Find each parasitized red blood cell.
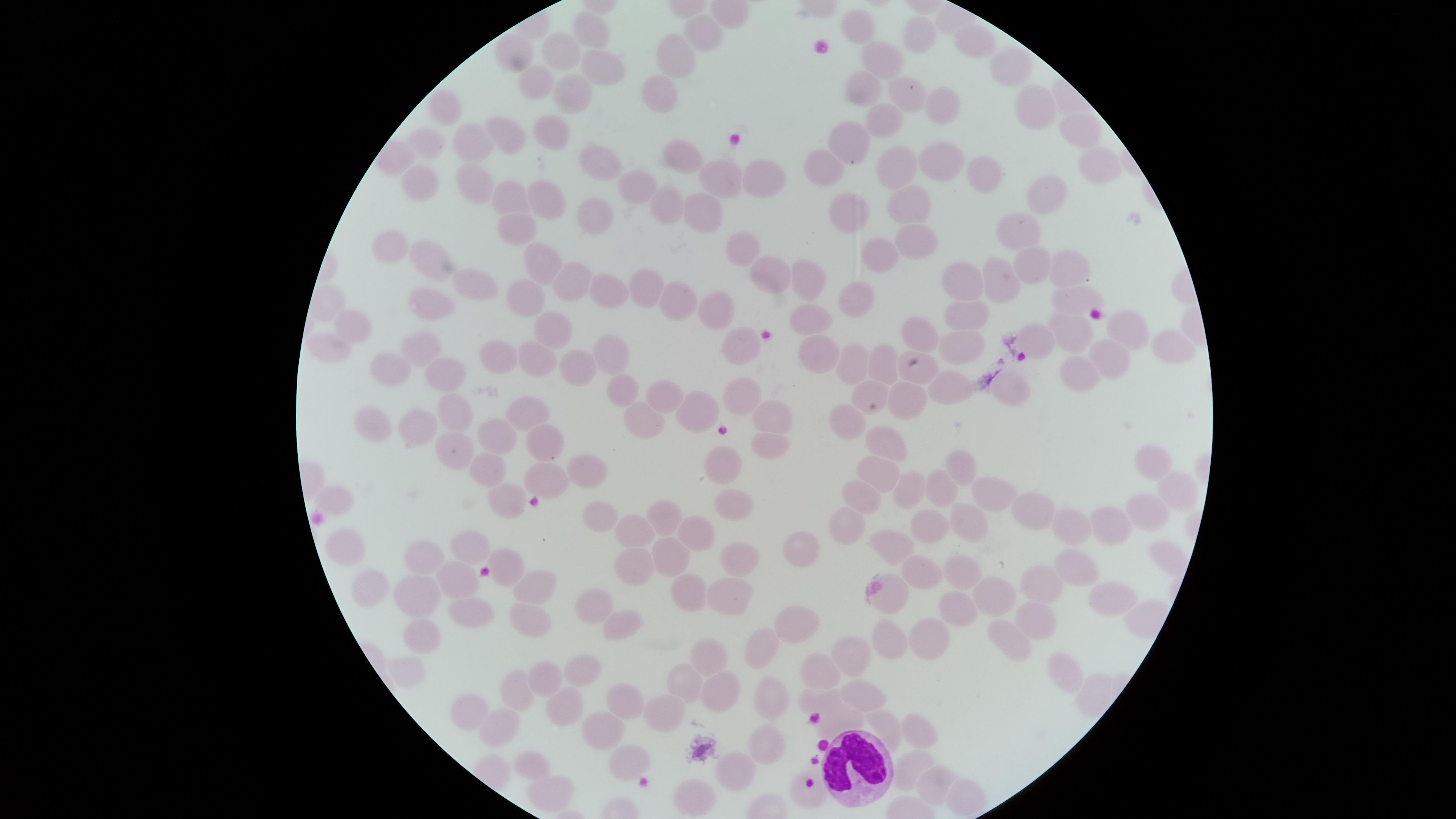
No parasitized red blood cells identified.

white blood cells = approximate marker points as {x, y} in pixels: {856, 768}
visible region = circular
field of view = single
capture = smartphone photograph through the microscope eyepiece
uninfected red blood cells = approximate marker points as {x, y} in pixels: {862, 23}, {702, 33}, {590, 34}, {915, 36}, {973, 41}, {556, 50}, {518, 51}, {678, 56}, {880, 58}, {999, 61}, {603, 64}, {660, 83}, {531, 84}, {865, 91}, {902, 91}, {565, 95}, {445, 102}, {1029, 102}, {929, 103}, {885, 118}, {553, 130}, {1076, 131}, {859, 137}, {428, 140}, {473, 141}, {508, 142}, {678, 147}, {897, 158}, {939, 159}, {833, 163}, {599, 164}, {761, 167}, {980, 170}, {718, 171}, {419, 179}, {473, 180}, {635, 182}, {1049, 193}, {514, 195}, {669, 198}, {544, 200}, {857, 206}, {910, 206}, {704, 207}, {596, 212}, {517, 226}, {1018, 226}, {910, 239}, {741, 245}, {393, 248}, {877, 256}, {428, 258}, {545, 262}, {1035, 265}, {1069, 265}, {763, 269}, {809, 272}, {964, 278}, {1001, 278}, {572, 281}, {483, 282}, {650, 287}, {613, 288}, {522, 295}, {1071, 295}, {856, 297}, {427, 300}, {680, 304}, {715, 306}, {963, 316}, {811, 317}, {1124, 326}, {555, 327}, {917, 328}, {353, 329}, {1077, 333}, {1037, 337}, {953, 338}, {740, 339}, {420, 342}, {1165, 342}, {329, 345}, {618, 350}, {1119, 351}, {531, 354}, {816, 355}, {494, 359}, {880, 361}, {852, 363}, {395, 365}, {578, 365}, {920, 369}, {450, 371}, {1081, 373}, {952, 381}, {619, 388}, {873, 389}, {1014, 389}, {746, 390}, {661, 396}, {910, 397}, {527, 411}, {455, 412}, {693, 412}, {770, 416}, {637, 419}, {846, 421}, {422, 427}, {370, 429}, {882, 436}, {492, 438}, {453, 442}, {544, 443}, {766, 449}, {1152, 461}, {486, 465}, {718, 465}, {971, 469}, {584, 470}, {875, 472}, {546, 477}, {899, 490}, {332, 493}, {939, 493}, {1171, 493}, {1002, 497}, {507, 498}, {859, 500}, {732, 504}, {592, 507}, {1140, 507}, {1034, 509}, {663, 515}, {843, 525}, {927, 525}, {967, 525}, {1113, 525}, {1074, 528}, {697, 531}, {630, 537}, {341, 542}, {890, 543}, {467, 548}, {807, 549}, {419, 554}, {673, 554}, {735, 554}, {1075, 562}, {505, 564}, {627, 568}, {923, 571}, {962, 573}, {455, 583}, {370, 585}, {1043, 587}, {531, 589}, {692, 591}, {727, 592}, {886, 592}, {994, 599}, {1109, 599}, {422, 602}, {590, 605}, {950, 612}, {464, 613}, {799, 620}, {1034, 620}, {525, 621}, {621, 626}, {931, 635}, {421, 636}, {894, 641}, {1008, 642}, {758, 645}, {855, 652}, {711, 654}, {1067, 665}, {582, 668}, {822, 670}, {689, 675}, {546, 677}, {721, 688}, {862, 693}, {519, 695}, {824, 695}, {771, 699}, {620, 700}, {561, 707}, {472, 715}, {655, 716}, {603, 724}, {839, 724}, {886, 727}, {497, 728}, {913, 733}, {765, 745}, {625, 761}, {911, 764}, {534, 768}, {734, 769}, {935, 785}, {551, 790}, {695, 792}, {812, 794}, {955, 801}
stain = Giemsa
image size = 1456×819 pixels
preparation = thin blood film